Locate every blood parasite and identify its species.
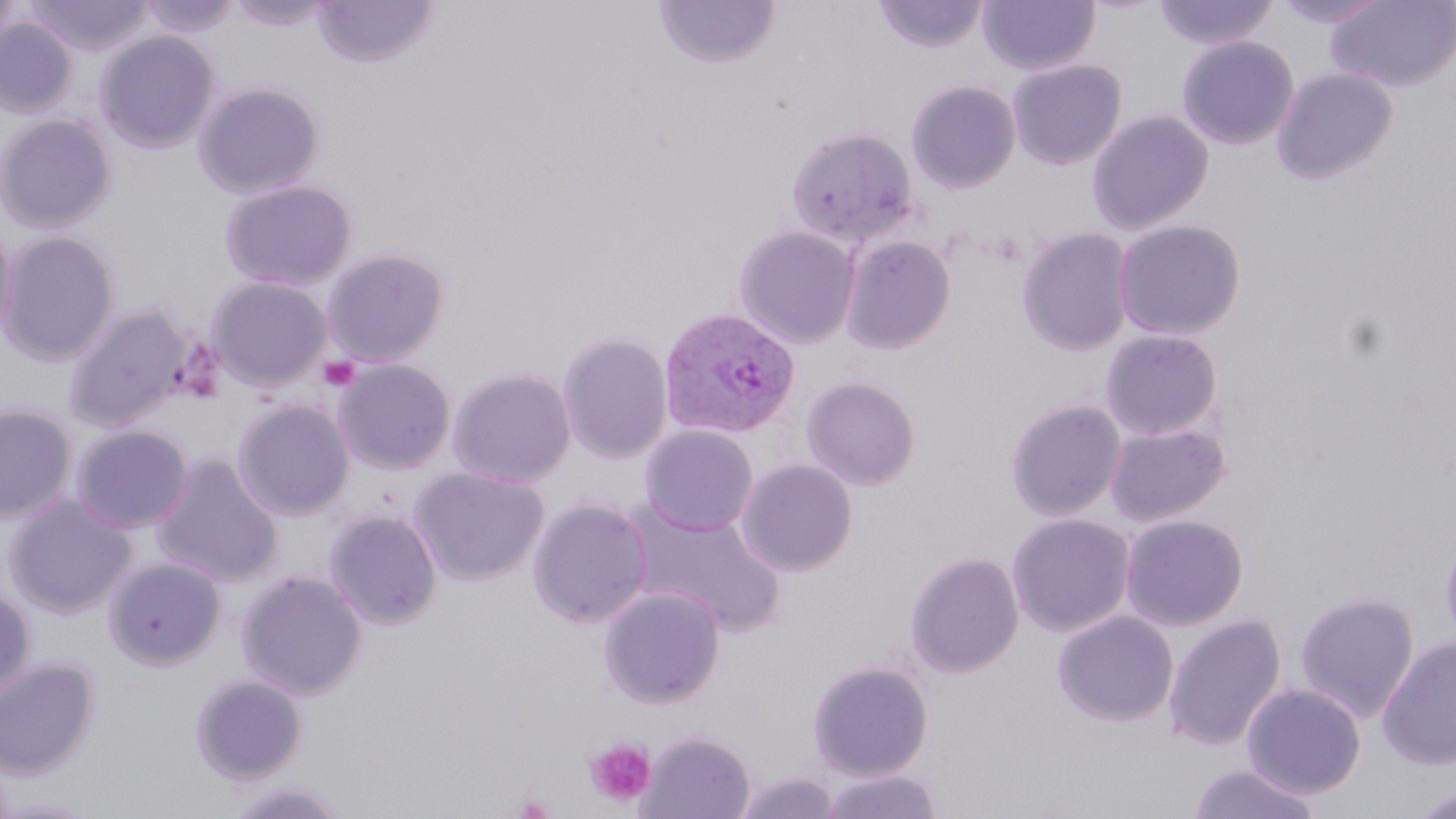
Approximate bounding boxes as named x1/y1/x2/y2 corners in pixels.
Plasmodium vivax-infected red blood cells: (x1=658, y1=307, x2=800, y2=439).
No Plasmodium falciparum, Plasmodium ovale, Plasmodium malariae, Babesia divergens, or Trypanosoma brucei observed.

slide-level diagnosis = Plasmodium vivax
platelet locations = approximate bounding boxes as named x1/y1/x2/y2 corners in pixels: (x1=318, y1=356, x2=361, y2=392), (x1=585, y1=738, x2=657, y2=807)
magnification = 1000x
uninfected red blood cell locations = approximate bounding boxes as named x1/y1/x2/y2 corners in pixels: (x1=0, y1=0, x2=21, y2=64), (x1=21, y1=0, x2=155, y2=57), (x1=137, y1=0, x2=243, y2=39), (x1=222, y1=0, x2=337, y2=31), (x1=312, y1=0, x2=438, y2=68), (x1=654, y1=0, x2=780, y2=69), (x1=872, y1=0, x2=989, y2=54), (x1=977, y1=0, x2=1101, y2=76), (x1=1152, y1=0, x2=1279, y2=51), (x1=1271, y1=0, x2=1388, y2=29), (x1=1326, y1=0, x2=1456, y2=92), (x1=0, y1=17, x2=77, y2=118), (x1=95, y1=29, x2=221, y2=154), (x1=1176, y1=35, x2=1300, y2=150), (x1=1007, y1=58, x2=1128, y2=170), (x1=1270, y1=67, x2=1398, y2=185), (x1=906, y1=80, x2=1021, y2=193), (x1=193, y1=81, x2=325, y2=198), (x1=1087, y1=109, x2=1214, y2=234), (x1=0, y1=113, x2=118, y2=233), (x1=785, y1=125, x2=920, y2=247), (x1=219, y1=178, x2=358, y2=291), (x1=1112, y1=219, x2=1247, y2=340), (x1=0, y1=221, x2=18, y2=346), (x1=733, y1=224, x2=862, y2=348), (x1=1016, y1=226, x2=1136, y2=356), (x1=0, y1=229, x2=121, y2=365), (x1=840, y1=234, x2=957, y2=354), (x1=321, y1=247, x2=450, y2=367), (x1=210, y1=264, x2=450, y2=377), (x1=206, y1=275, x2=333, y2=391), (x1=63, y1=303, x2=193, y2=432), (x1=1100, y1=328, x2=1223, y2=441), (x1=556, y1=331, x2=673, y2=464), (x1=333, y1=358, x2=457, y2=474), (x1=447, y1=367, x2=576, y2=488), (x1=800, y1=375, x2=922, y2=491), (x1=232, y1=398, x2=355, y2=520), (x1=1005, y1=398, x2=1126, y2=521), (x1=0, y1=403, x2=78, y2=524), (x1=1104, y1=421, x2=1230, y2=526), (x1=70, y1=423, x2=194, y2=533), (x1=640, y1=424, x2=759, y2=535), (x1=150, y1=453, x2=285, y2=587), (x1=735, y1=458, x2=858, y2=576), (x1=409, y1=466, x2=549, y2=586), (x1=2, y1=493, x2=138, y2=618), (x1=526, y1=496, x2=653, y2=628), (x1=623, y1=501, x2=787, y2=637), (x1=324, y1=509, x2=443, y2=630), (x1=1006, y1=513, x2=1135, y2=636), (x1=1120, y1=514, x2=1249, y2=630), (x1=1440, y1=524, x2=1456, y2=657), (x1=904, y1=552, x2=1024, y2=678), (x1=104, y1=556, x2=226, y2=670), (x1=236, y1=569, x2=368, y2=700), (x1=598, y1=585, x2=726, y2=708), (x1=0, y1=587, x2=35, y2=702), (x1=1295, y1=591, x2=1420, y2=722), (x1=1052, y1=610, x2=1179, y2=727), (x1=1162, y1=614, x2=1286, y2=751), (x1=1377, y1=635, x2=1456, y2=770), (x1=0, y1=658, x2=99, y2=779), (x1=807, y1=660, x2=934, y2=780), (x1=189, y1=673, x2=308, y2=785), (x1=1242, y1=682, x2=1367, y2=799), (x1=638, y1=729, x2=756, y2=819), (x1=1188, y1=762, x2=1323, y2=819), (x1=819, y1=768, x2=943, y2=819), (x1=736, y1=770, x2=841, y2=818), (x1=222, y1=780, x2=349, y2=818), (x1=1412, y1=785, x2=1456, y2=819), (x1=0, y1=797, x2=101, y2=818)
preparation = thin blood smear
modality = light microscopy
image size = 1456×819 pixels
stain = May-Grünwald-Giemsa
field of view = one of a larger specimen